Name the cell type shown.
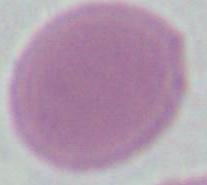
This is an erythrocyte.

Summary:
  - Modality: photomicrograph
  - Magnification: 1000x